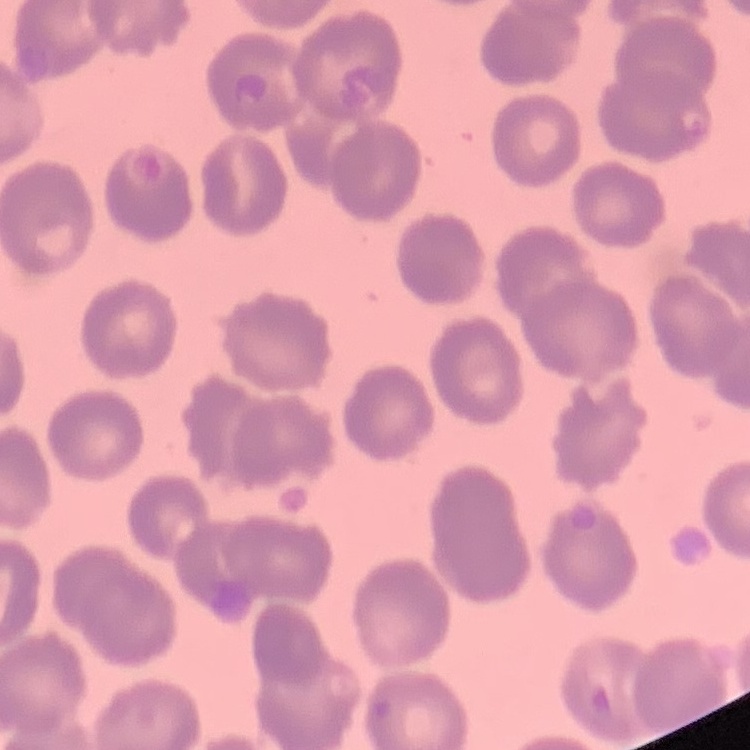

{
  "red_blood_cell_morphology": "no rouleaux formation",
  "image_type": "square crop of a larger photomicrograph",
  "stain": "Field's or Giemsa",
  "preparation": "thin peripheral smear"
}